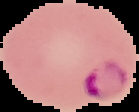 Segmented cell region on a black background. Image is 139×112 pixels. Result: malaria parasites detected. From a thin blood smear.